Assess this cell for malaria.
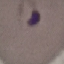

It is parasitized.

{
  "preparation": "thin blood film",
  "capture": "smartphone through the microscope eyepiece",
  "image_type": "automatically extracted cell patch, resized to 64 × 64 pixels",
  "stain": "Giemsa"
}